Classify this cell by malaria status.
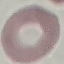
It is uninfected.

{
  "image_type": "automatically extracted cell patch, resized to 64 × 64 pixels",
  "preparation": "thin smear",
  "capture": "smartphone through the microscope eyepiece",
  "stain": "Giemsa"
}